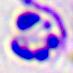
Summary:
  - Identification: white blood cell
  - Modality: photomicrograph
  - Magnification: 400x